Comment on the morphology of the erythrocytes.
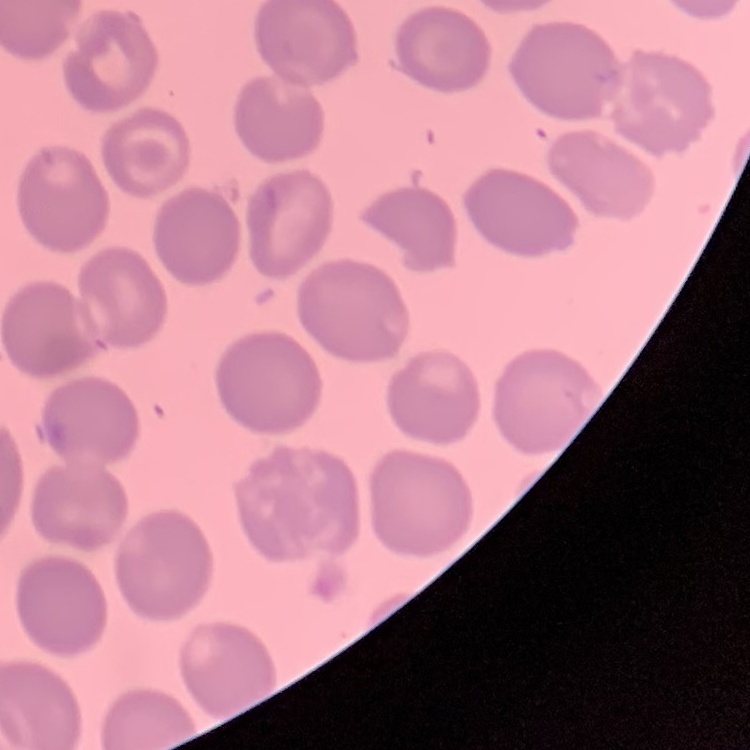

No rouleaux formation.

Thin blood smear. Field's or Giemsa stain. One tile cut from a larger photomicrograph.